Classify this cell by malaria status.
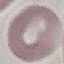
It is uninfected.

Summary:
  - Stain: Giemsa
  - Capture: smartphone through the microscope eyepiece
  - Image type: automatically extracted cell patch, resized to 64 × 64 pixels
  - Preparation: thin blood smear